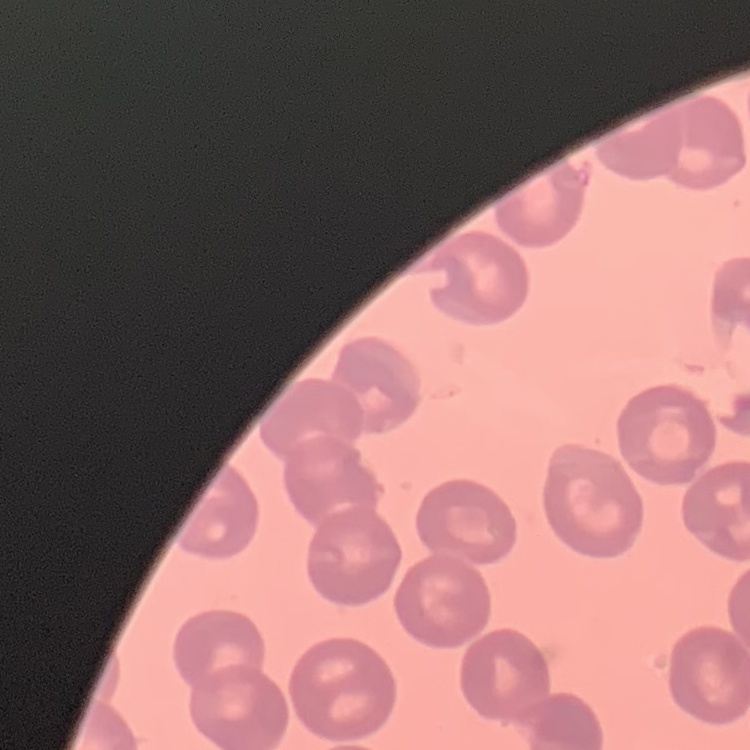
Summary:
  - Red blood cell morphology: no rouleaux formation
  - Image type: square crop of a larger photomicrograph
  - Stain: Field's or Giemsa
  - Preparation: thin blood film